State which parasite is depicted.
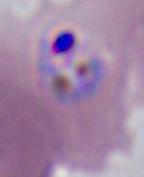
This is Plasmodium.

magnification: 400x or 1000x
modality: photomicrograph